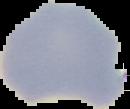
image type = segmented cell region with the area outside set to black
image size = 130×109 pixels
result = no Plasmodium parasites detected
preparation = thin blood film